Assess this cell for malaria.
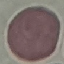
It is uninfected.

Summary:
  - Capture: smartphone through the microscope eyepiece
  - Preparation: thin smear
  - Stain: Giemsa
  - Image type: cell patch, automatically extracted from a larger field of view and resized to 64 × 64 pixels